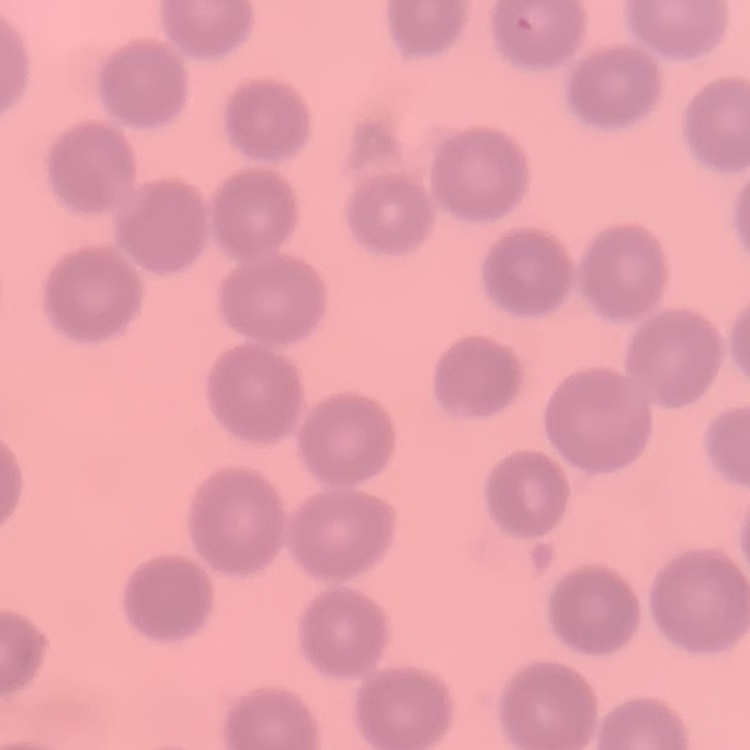

The red blood cells show no rouleaux formation. Thin blood film. One tile cut from a larger photomicrograph. Field's or Giemsa stain.